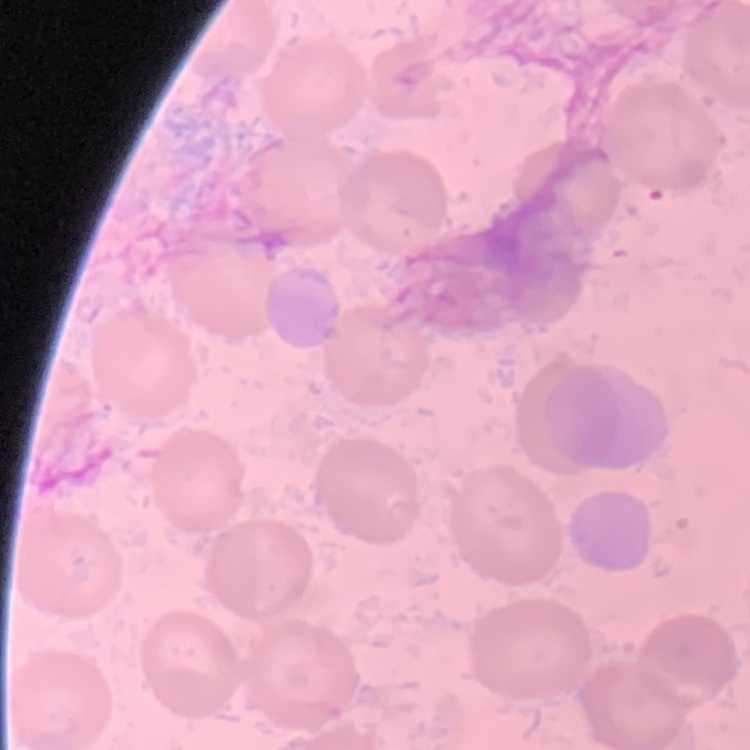
Summary:
  - Red blood cell morphology: no rouleaux formation
  - Image type: one tile cut from a larger photomicrograph
  - Preparation: thin blood film
  - Stain: Field's or Giemsa